Assess this cell for malaria.
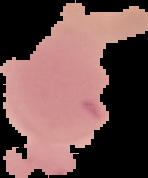
It is uninfected.

Image is 148×178 pixels. From a thin blood smear. The area outside the segmented cell region is set to black.